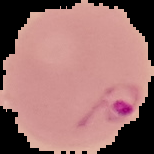
Image is 154×154 pixels. Result: malaria parasites detected. The area outside the segmented cell region is set to black. From a thin blood film.